State which parasite is depicted.
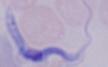

A trypanosome.

modality = micrograph
magnification = 1000x